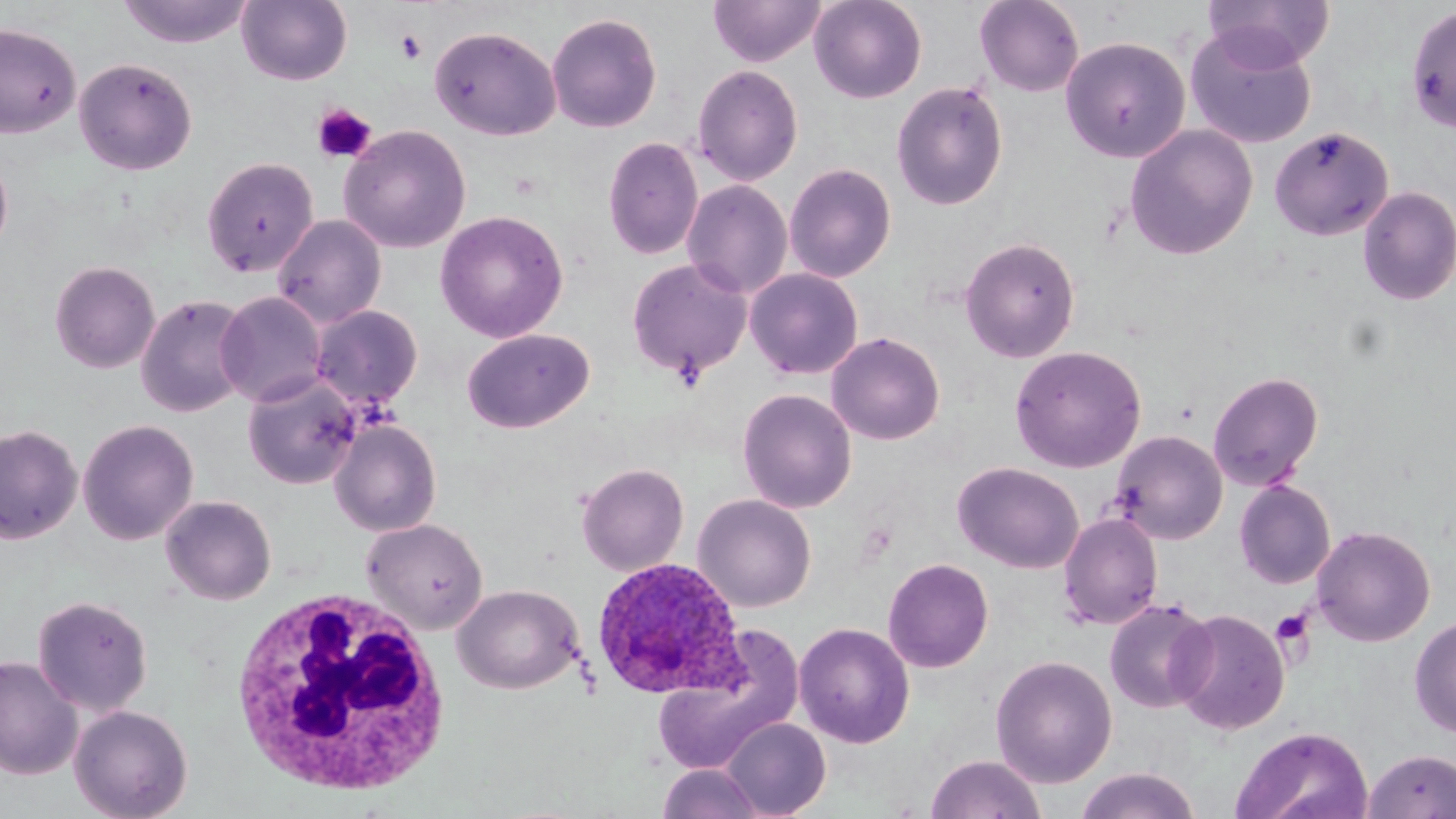

Summary:
  - Coordinate format: approximate bounding boxes as (x1, y1, x2, y2) in pixels
  - Platelet locations: (396, 29, 427, 64), (312, 103, 377, 164), (1271, 609, 1315, 654)
  - Plasmodium ovale-infected red blood cell locations: (590, 557, 745, 699)
  - Uninfected red blood cell locations: (118, 0, 254, 48), (237, 0, 352, 86), (708, 0, 826, 67), (809, 0, 927, 104), (975, 0, 1084, 97), (1202, 0, 1336, 71), (699, 1, 918, 80), (1405, 5, 1456, 133), (546, 12, 663, 133), (0, 22, 81, 139), (429, 25, 561, 141), (1185, 26, 1318, 148), (1060, 36, 1190, 162), (73, 57, 198, 175), (692, 63, 804, 186), (891, 80, 1009, 210), (1124, 123, 1258, 260), (339, 125, 471, 253), (1269, 125, 1393, 241), (603, 136, 703, 260), (0, 150, 14, 261), (201, 156, 318, 277), (784, 163, 896, 282), (682, 179, 793, 300), (1357, 186, 1456, 306), (435, 210, 568, 342), (273, 214, 387, 328), (959, 236, 1081, 363), (626, 257, 753, 381), (49, 260, 160, 374), (745, 268, 863, 380), (216, 291, 328, 408), (136, 294, 253, 417), (311, 304, 423, 411), (461, 328, 594, 433), (826, 332, 945, 445), (1009, 345, 1146, 473), (1207, 371, 1324, 490), (242, 372, 362, 489), (737, 388, 857, 513), (328, 418, 442, 537), (78, 419, 199, 545), (0, 424, 83, 545), (1111, 430, 1228, 545), (576, 462, 690, 576), (953, 462, 1084, 573), (1234, 479, 1335, 589), (161, 494, 277, 605), (692, 494, 816, 612), (1058, 512, 1163, 630), (362, 517, 489, 634), (1311, 525, 1436, 647), (882, 558, 994, 672), (452, 583, 584, 694), (32, 594, 154, 717), (1104, 598, 1217, 714), (1171, 609, 1290, 735), (1410, 616, 1456, 739), (793, 622, 915, 748), (652, 630, 799, 776), (0, 654, 83, 781), (990, 655, 1118, 788), (69, 704, 193, 819), (720, 717, 831, 817), (1231, 725, 1374, 819), (1362, 748, 1456, 819), (925, 753, 1047, 818), (657, 763, 765, 819), (1075, 767, 1201, 819)
  - White blood cell locations: (227, 588, 455, 800)
  - Slide-level diagnosis: Plasmodium ovale
  - Magnification: 1000x
  - Image size: 1456×819 pixels
  - Field of view: one of a larger specimen
  - Preparation: thin blood film
  - Modality: optical microscopy
  - Stain: May-Grünwald-Giemsa